Assess this cell for malaria.
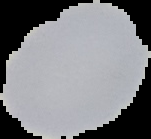
Uninfected.

image_size: 151×139 pixels
preparation: thin blood film
image_type: segmented cell region on a black background